Locate every blood parasite and identify its species.
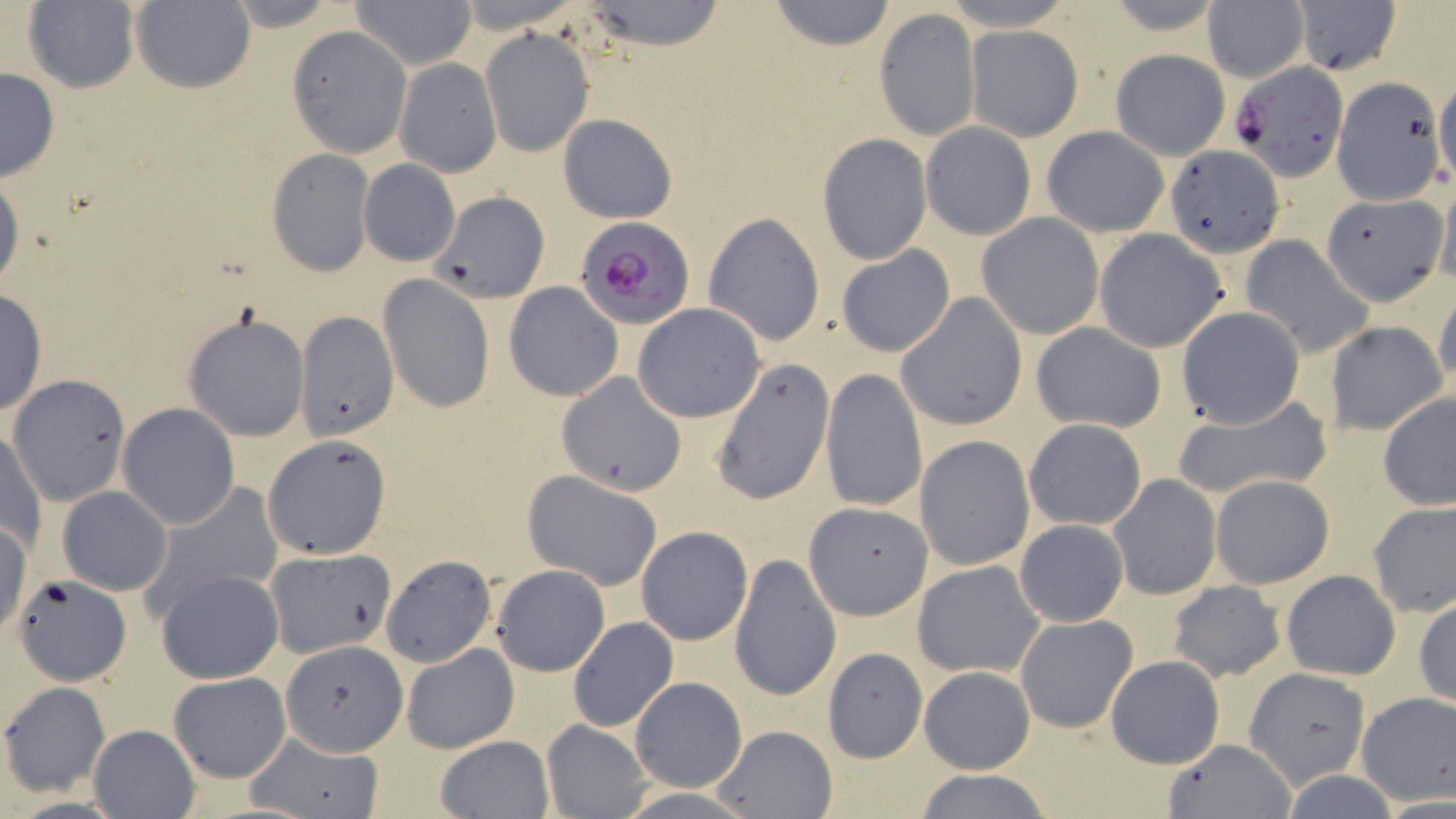
Approximate bounding boxes as named x1/y1/x2/y2 corners in pixels.
Plasmodium falciparum-infected red blood cells: (x1=1232, y1=62, x2=1348, y2=179), (x1=576, y1=217, x2=695, y2=330).
No Plasmodium ovale, Plasmodium malariae, Plasmodium vivax, Babesia divergens, or Trypanosoma brucei observed.

Summary:
  - Uninfected red blood cell locations: (x1=23, y1=0, x2=141, y2=93), (x1=132, y1=0, x2=255, y2=93), (x1=219, y1=0, x2=346, y2=30), (x1=353, y1=0, x2=475, y2=67), (x1=578, y1=0, x2=728, y2=49), (x1=768, y1=0, x2=897, y2=51), (x1=1202, y1=1, x2=1308, y2=82), (x1=1291, y1=1, x2=1402, y2=76), (x1=873, y1=7, x2=982, y2=143), (x1=287, y1=26, x2=412, y2=156), (x1=968, y1=26, x2=1081, y2=141), (x1=480, y1=27, x2=594, y2=157), (x1=1110, y1=50, x2=1229, y2=159), (x1=394, y1=58, x2=500, y2=176), (x1=0, y1=67, x2=60, y2=181), (x1=1432, y1=77, x2=1456, y2=185), (x1=1331, y1=78, x2=1446, y2=206), (x1=557, y1=112, x2=677, y2=222), (x1=920, y1=122, x2=1035, y2=239), (x1=1042, y1=126, x2=1169, y2=237), (x1=816, y1=132, x2=931, y2=264), (x1=1166, y1=144, x2=1284, y2=257), (x1=265, y1=148, x2=375, y2=276), (x1=359, y1=160, x2=460, y2=266), (x1=0, y1=169, x2=24, y2=296), (x1=1433, y1=179, x2=1456, y2=294), (x1=430, y1=193, x2=550, y2=304), (x1=1321, y1=195, x2=1446, y2=306), (x1=703, y1=211, x2=826, y2=347), (x1=977, y1=213, x2=1103, y2=340), (x1=1094, y1=228, x2=1231, y2=353), (x1=1238, y1=235, x2=1375, y2=358), (x1=835, y1=245, x2=955, y2=357), (x1=377, y1=273, x2=493, y2=413), (x1=504, y1=282, x2=625, y2=400), (x1=0, y1=286, x2=47, y2=420), (x1=1433, y1=287, x2=1456, y2=395), (x1=895, y1=293, x2=1026, y2=431), (x1=632, y1=303, x2=766, y2=422), (x1=1176, y1=306, x2=1305, y2=429), (x1=295, y1=310, x2=397, y2=440), (x1=182, y1=312, x2=312, y2=441), (x1=1324, y1=321, x2=1449, y2=434), (x1=1030, y1=322, x2=1168, y2=434), (x1=712, y1=357, x2=835, y2=506), (x1=821, y1=366, x2=929, y2=512), (x1=560, y1=370, x2=684, y2=496), (x1=9, y1=375, x2=129, y2=505), (x1=1378, y1=391, x2=1455, y2=511), (x1=1173, y1=393, x2=1331, y2=505), (x1=118, y1=403, x2=240, y2=529), (x1=1023, y1=417, x2=1147, y2=531), (x1=2, y1=428, x2=46, y2=557), (x1=262, y1=434, x2=393, y2=560), (x1=915, y1=435, x2=1036, y2=571), (x1=522, y1=470, x2=664, y2=589), (x1=1108, y1=474, x2=1221, y2=600), (x1=1210, y1=474, x2=1335, y2=589), (x1=139, y1=483, x2=283, y2=615), (x1=58, y1=486, x2=172, y2=596), (x1=802, y1=502, x2=932, y2=621), (x1=1368, y1=502, x2=1456, y2=615), (x1=1015, y1=519, x2=1128, y2=628), (x1=636, y1=526, x2=754, y2=646), (x1=264, y1=548, x2=398, y2=661), (x1=729, y1=552, x2=842, y2=703), (x1=380, y1=555, x2=496, y2=667), (x1=912, y1=560, x2=1047, y2=679), (x1=492, y1=564, x2=609, y2=676), (x1=156, y1=569, x2=284, y2=684), (x1=1281, y1=569, x2=1402, y2=680), (x1=11, y1=574, x2=131, y2=687), (x1=1167, y1=581, x2=1285, y2=680), (x1=1414, y1=595, x2=1456, y2=709), (x1=1015, y1=615, x2=1137, y2=734), (x1=568, y1=617, x2=678, y2=732), (x1=282, y1=637, x2=405, y2=761), (x1=401, y1=644, x2=520, y2=753), (x1=822, y1=647, x2=929, y2=762), (x1=1105, y1=655, x2=1225, y2=769), (x1=1243, y1=665, x2=1373, y2=790), (x1=920, y1=667, x2=1035, y2=774), (x1=168, y1=672, x2=290, y2=783), (x1=628, y1=676, x2=747, y2=792), (x1=2, y1=682, x2=111, y2=797), (x1=1355, y1=691, x2=1456, y2=806), (x1=541, y1=721, x2=652, y2=817), (x1=709, y1=723, x2=839, y2=818), (x1=87, y1=724, x2=199, y2=817), (x1=244, y1=732, x2=383, y2=818), (x1=435, y1=735, x2=552, y2=818), (x1=1162, y1=738, x2=1295, y2=818), (x1=913, y1=769, x2=1054, y2=819)
  - Slide-level diagnosis: Plasmodium falciparum
  - Magnification: 1000x
  - Stain: May-Grünwald-Giemsa
  - Preparation: thin blood film
  - Image size: 1456×819 pixels
  - Modality: light microscopy
  - Field of view: single